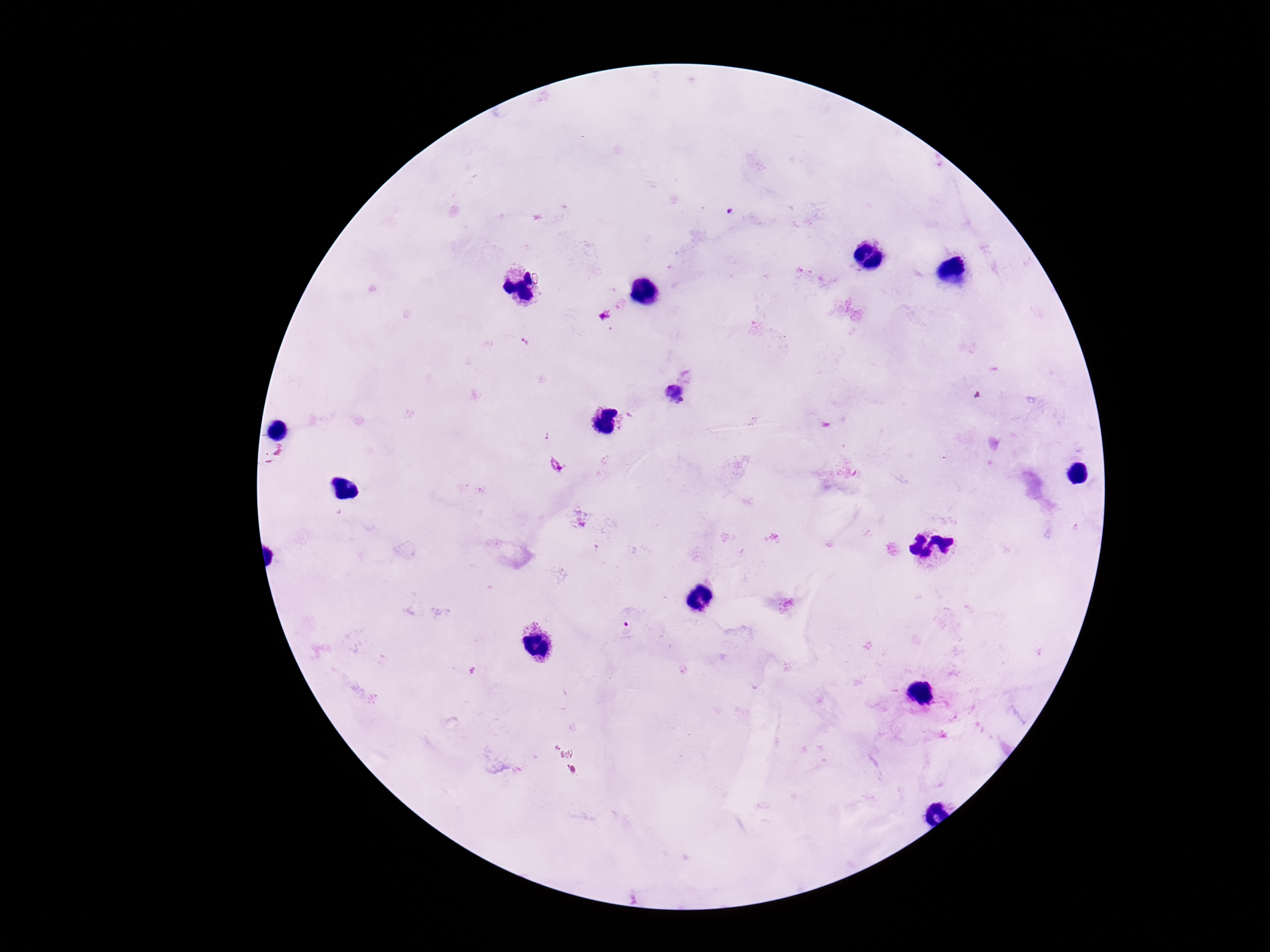
image size = 1270×952 pixels
magnification = 100x
patient malaria status = positive
stain = Giemsa
Plasmodium parasite locations = approximate centers as {x, y} in pixels: {729, 212}, {674, 394}, {631, 624}
field of view = single
capture = smartphone camera through the microscope eyepiece
preparation = thick peripheral-blood smear